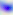 Micrograph. Captured at 400x magnification. Toxoplasma gondii is seen.